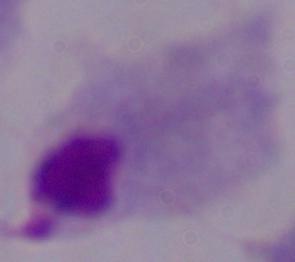
Summary:
  - Identification: trichomonad
  - Magnification: 1000x
  - Modality: photomicrograph